Report the malaria status of this cell.
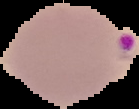

Parasitized.

{
  "image_type": "cell region segmented out of the field of view; surrounding area masked to black",
  "preparation": "thin blood film",
  "image_size": "139×109 pixels"
}